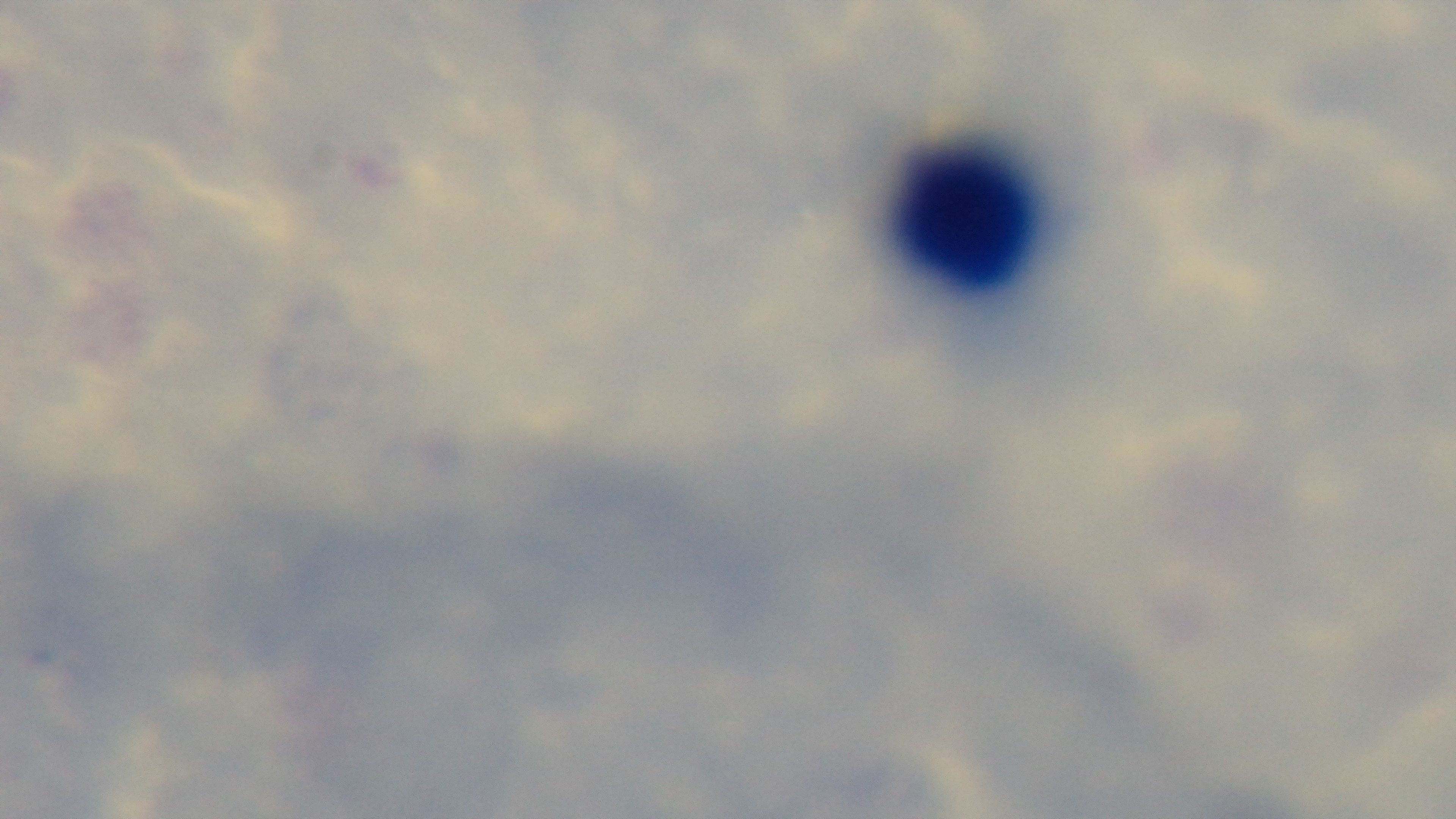
preparation = thick smear
modality = light microscopy
objective = 100x oil immersion
malaria status = negative
field of view = one from the slide
capture = mounted 4K digital camera
stain = Giemsa